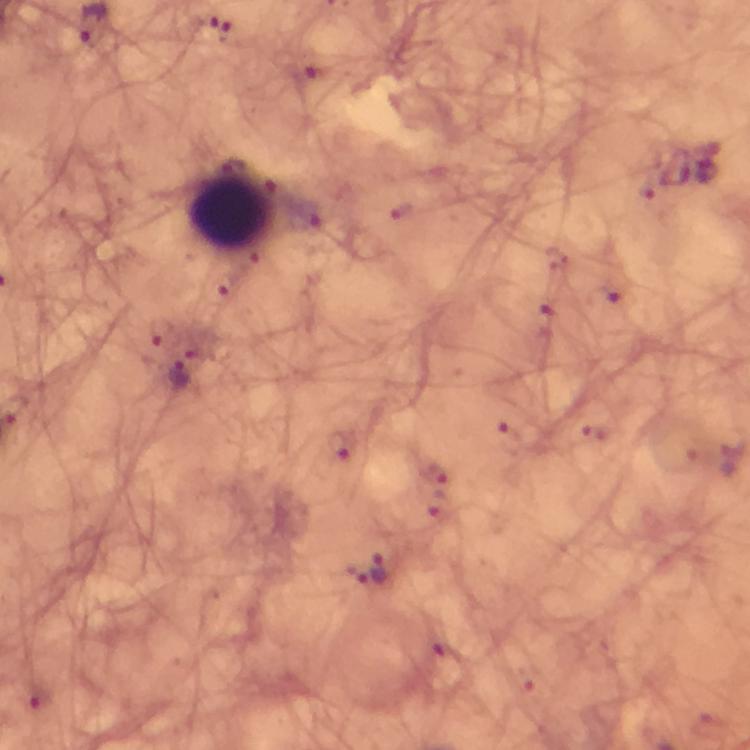
Approximate centers as {x, y} in pixels.
Summary:
  - Malaria parasite locations: {211, 26}, {307, 71}, {222, 287}, {604, 298}, {545, 319}, {161, 333}, {179, 373}, {339, 444}, {436, 472}, {435, 505}, {381, 569}, {39, 695}
  - Leukocyte locations: {232, 207}
  - Capture: smartphone mounted on the microscope
  - Image size: 750×750 pixels
  - Stain: Giemsa
  - Cropped from: one field of view
  - Immersion oil: applied
  - Magnification: 100x
  - Preparation: thick blood smear
  - Context: from a diagnostic examination for malaria